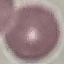
Result: no malaria parasites seen. Cell patch, automatically extracted from a larger field of view and resized to 64 × 64 pixels. Thin smear of blood. Acquired by smartphone through the microscope eyepiece. Giemsa stain.